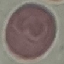
malaria status = uninfected
capture = smartphone camera at the microscope eyepiece
stain = Giemsa
image type = cell patch, automatically extracted from a larger field of view and resized to 64 × 64 pixels
preparation = thin smear